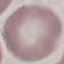

Malaria status: uninfected. Acquired by smartphone through the microscope eyepiece. Giemsa-stained preparation. Cell patch, automatically extracted from a larger field of view and resized to 64 × 64 pixels. Thin blood smear.